Outline each blood parasite and name the species.
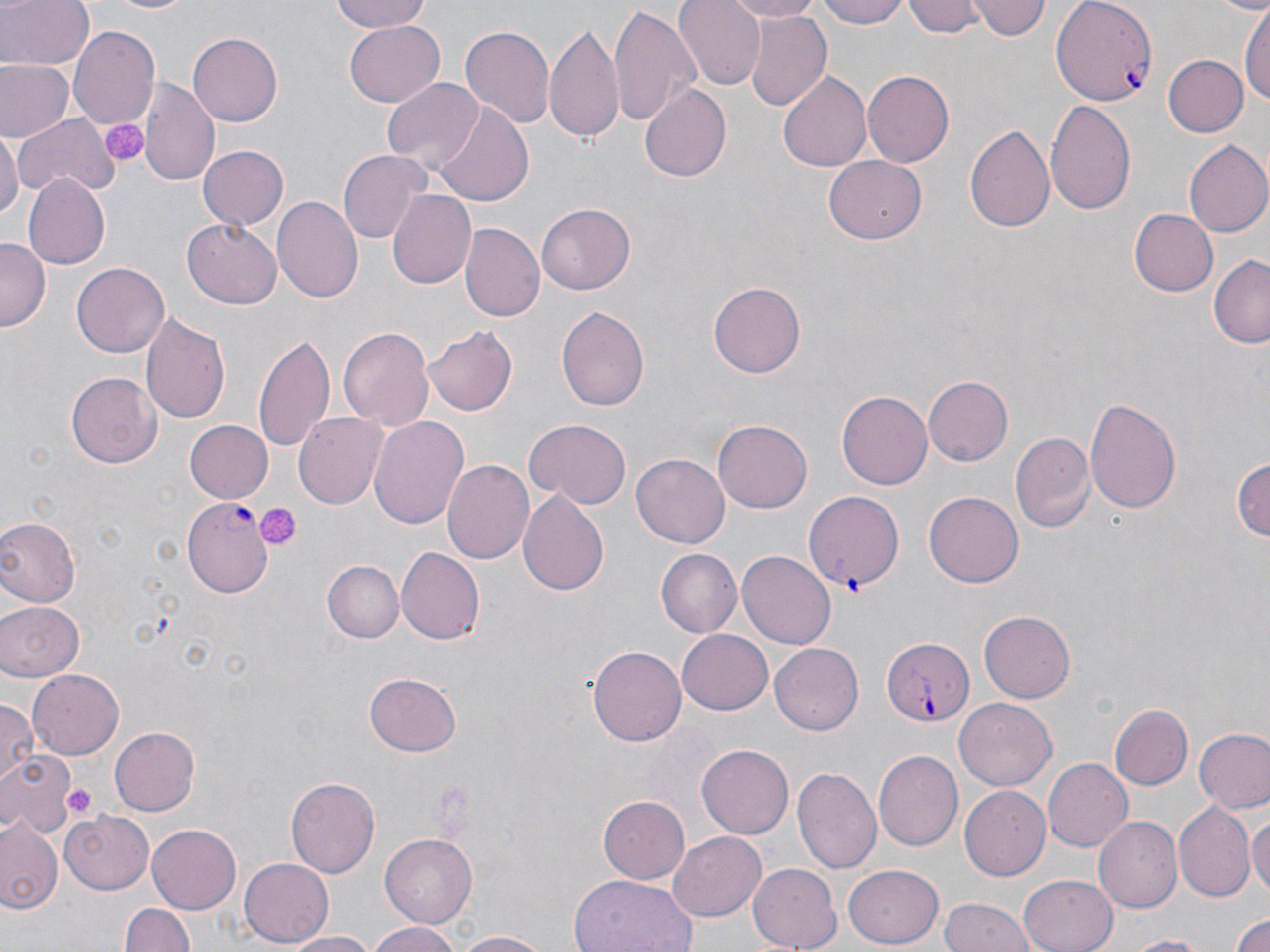
Approximate bounding boxes as (x1, y1, x2, y2) in pixels.
Plasmodium falciparum-infected red blood cells: (1051, 0, 1158, 106), (183, 498, 274, 599), (880, 635, 974, 727).
No Plasmodium ovale, Plasmodium malariae, Plasmodium vivax, Babesia divergens, or Trypanosoma brucei observed.

Platelet locations: (102, 121, 148, 166), (256, 503, 299, 550), (837, 565, 868, 595), (65, 785, 95, 819). Uninfected red blood cell locations: (0, 0, 94, 73), (100, 0, 199, 16), (327, 0, 438, 33), (674, 0, 764, 90), (717, 0, 826, 21), (821, 0, 914, 27), (905, 0, 986, 38), (969, 0, 1050, 43), (1240, 2, 1268, 113), (608, 5, 698, 131), (743, 11, 831, 113), (545, 20, 626, 148), (345, 21, 445, 107), (461, 22, 554, 131), (69, 25, 161, 129), (189, 34, 281, 124), (1160, 54, 1250, 140), (1, 60, 71, 140), (862, 70, 953, 168), (777, 71, 874, 174), (383, 76, 484, 171), (139, 77, 217, 188), (641, 84, 732, 182), (1044, 100, 1136, 217), (432, 102, 533, 208), (15, 113, 119, 198), (964, 122, 1055, 233), (0, 126, 21, 221), (1184, 139, 1270, 238), (198, 143, 289, 232), (340, 149, 429, 244), (826, 154, 927, 243), (24, 175, 110, 269), (387, 189, 476, 289), (273, 195, 365, 303), (536, 203, 635, 294), (1128, 208, 1218, 296), (181, 218, 281, 308), (460, 220, 543, 323), (0, 238, 48, 332), (1208, 255, 1270, 348), (71, 262, 169, 358), (707, 282, 805, 379), (557, 304, 652, 412), (140, 312, 232, 424), (424, 324, 518, 416), (340, 326, 435, 431), (253, 330, 337, 456), (68, 371, 160, 467), (924, 375, 1013, 465), (837, 390, 931, 492), (1086, 395, 1182, 517), (294, 409, 388, 506), (369, 416, 470, 532), (524, 418, 631, 508), (714, 419, 815, 513), (184, 420, 272, 503), (1010, 431, 1096, 532), (633, 452, 730, 548), (1233, 454, 1268, 546), (443, 459, 534, 564), (518, 489, 610, 596), (805, 490, 905, 592), (925, 490, 1023, 584), (0, 518, 78, 608), (396, 548, 484, 645), (658, 548, 744, 639), (738, 550, 835, 649), (321, 560, 402, 643), (0, 596, 86, 680), (980, 610, 1074, 703), (676, 628, 774, 714), (770, 642, 863, 735), (587, 644, 686, 747), (26, 670, 122, 759), (364, 673, 462, 757), (956, 695, 1056, 789), (0, 700, 38, 789), (1109, 704, 1192, 790), (107, 726, 201, 817), (1193, 728, 1270, 813), (696, 744, 794, 839), (873, 748, 965, 851), (0, 751, 76, 836), (1042, 757, 1133, 852), (792, 767, 880, 876), (286, 777, 380, 877), (959, 786, 1051, 880), (598, 793, 690, 881), (1174, 803, 1254, 904), (63, 808, 151, 892), (1249, 809, 1270, 903), (1092, 815, 1182, 913), (0, 818, 62, 917), (147, 824, 242, 915), (669, 831, 767, 920), (381, 833, 481, 927), (239, 858, 334, 947), (746, 862, 842, 951), (842, 865, 945, 948), (1020, 872, 1118, 952), (567, 875, 698, 952), (941, 896, 1038, 952), (122, 900, 194, 952), (1227, 908, 1270, 952), (363, 921, 467, 952), (450, 930, 558, 951), (284, 931, 379, 951), (1121, 933, 1219, 952). Slide-level diagnosis: Plasmodium falciparum. Thin blood smear. 1000x magnification. Light microscopy. One field of a larger specimen. May-Grünwald-Giemsa stain. Image is 1270×952 pixels.